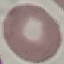

Summary:
  - Result: no malaria parasites detected
  - Preparation: thin blood smear
  - Stain: Giemsa
  - Capture: smartphone through the microscope eyepiece
  - Image type: cell patch, automatically extracted from a larger field of view and resized to 64 × 64 pixels